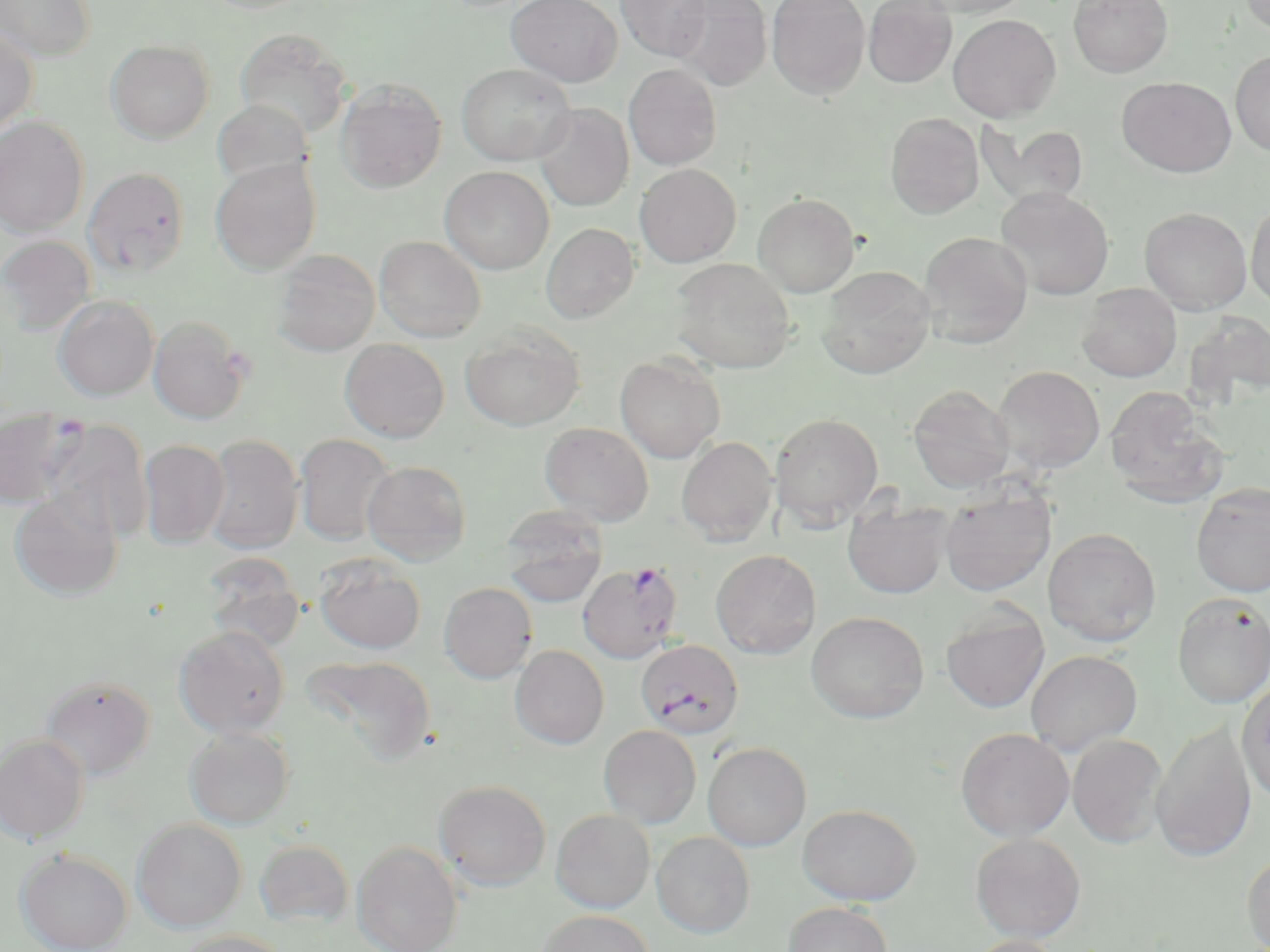

Approximate bounding boxes as (x1,y1)-(x2,y2) corner pairs in pixels. Uninfected red blood cell locations: (0,0)-(96,62), (507,0)-(622,87), (616,0)-(712,61), (671,0)-(772,91), (766,0)-(870,99), (918,0)-(1033,17), (1068,0)-(1174,77), (1240,0)-(1270,35), (863,1)-(957,87), (948,14)-(1061,122), (0,26)-(39,135), (235,28)-(351,137), (105,39)-(214,143), (1230,51)-(1270,156), (457,63)-(576,165), (624,63)-(722,170), (1119,77)-(1235,177), (336,79)-(446,193), (211,99)-(315,190), (533,104)-(634,211), (885,112)-(984,219), (0,116)-(89,238), (977,120)-(1090,208), (211,158)-(321,275), (635,164)-(741,267), (439,166)-(554,274), (83,167)-(190,277), (995,187)-(1115,300), (753,192)-(860,297), (1246,199)-(1270,311), (1139,207)-(1252,314), (541,223)-(639,323), (918,231)-(1033,348), (0,235)-(96,335), (374,236)-(486,342), (272,248)-(381,356), (670,258)-(796,373), (816,265)-(935,379), (1076,283)-(1182,382), (52,295)-(159,400), (1184,311)-(1270,408), (148,314)-(251,424), (460,324)-(585,431), (340,339)-(450,442), (615,353)-(725,463), (991,365)-(1105,474), (908,384)-(1015,493), (1104,386)-(1230,509), (0,407)-(83,508), (770,412)-(884,529), (41,418)-(153,542), (540,422)-(654,526), (294,433)-(396,545), (202,434)-(304,555), (676,436)-(778,545), (138,439)-(230,548), (362,460)-(472,565), (1191,482)-(1270,597), (939,483)-(1056,597), (9,490)-(123,600), (842,496)-(953,598), (500,507)-(608,607), (1043,527)-(1162,646), (710,549)-(821,659), (199,553)-(305,651), (314,554)-(426,654), (439,582)-(537,683), (1171,592)-(1270,708), (940,603)-(1050,713), (806,611)-(929,723), (174,625)-(291,738), (510,645)-(609,749), (1025,650)-(1143,756), (302,655)-(436,765), (40,676)-(156,779), (1236,677)-(1270,804), (1151,719)-(1256,863), (598,725)-(701,828), (184,727)-(294,830), (956,727)-(1075,842), (0,734)-(90,844), (1067,734)-(1169,848), (703,742)-(811,851), (434,779)-(551,891), (797,804)-(921,905), (551,809)-(655,912), (131,818)-(247,932), (651,831)-(756,938), (970,833)-(1086,943), (254,839)-(354,927), (352,840)-(463,952), (16,849)-(132,952), (1241,849)-(1270,952), (782,902)-(893,952), (536,910)-(654,952), (174,930)-(294,952), (963,935)-(1068,952). Plasmodium falciparum-infected red blood cell locations: (576,560)-(683,664), (634,639)-(744,742). Slide-level diagnosis: Plasmodium falciparum. Light microscopy. 1000x magnification. Thin blood film. Image is 1270×952 pixels. Single field of view. May-Grünwald-Giemsa-stained preparation.